Describe the morphology of the red blood cells.
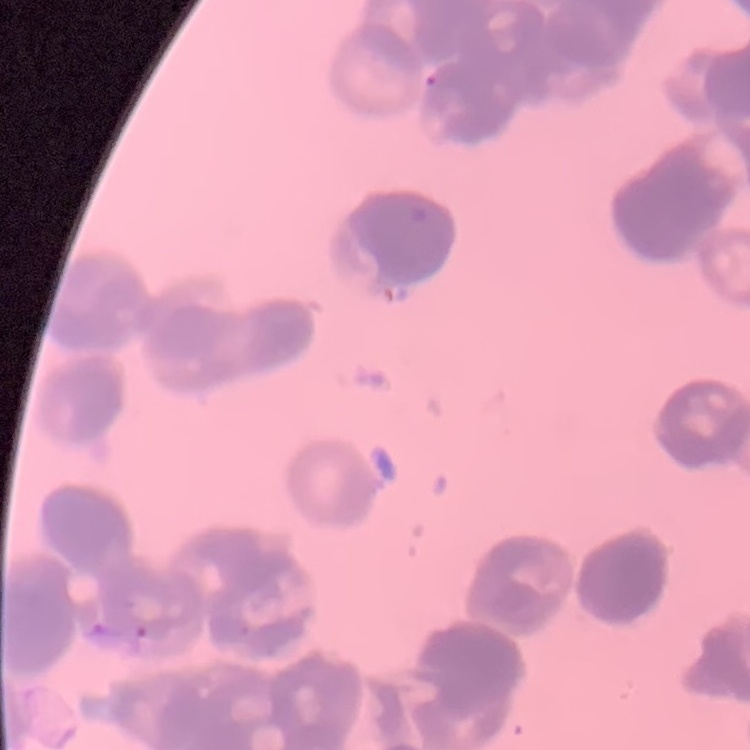
Rouleaux formation.

preparation: thin blood film
stain: Field's or Giemsa
image_type: one tile cut from a larger photomicrograph